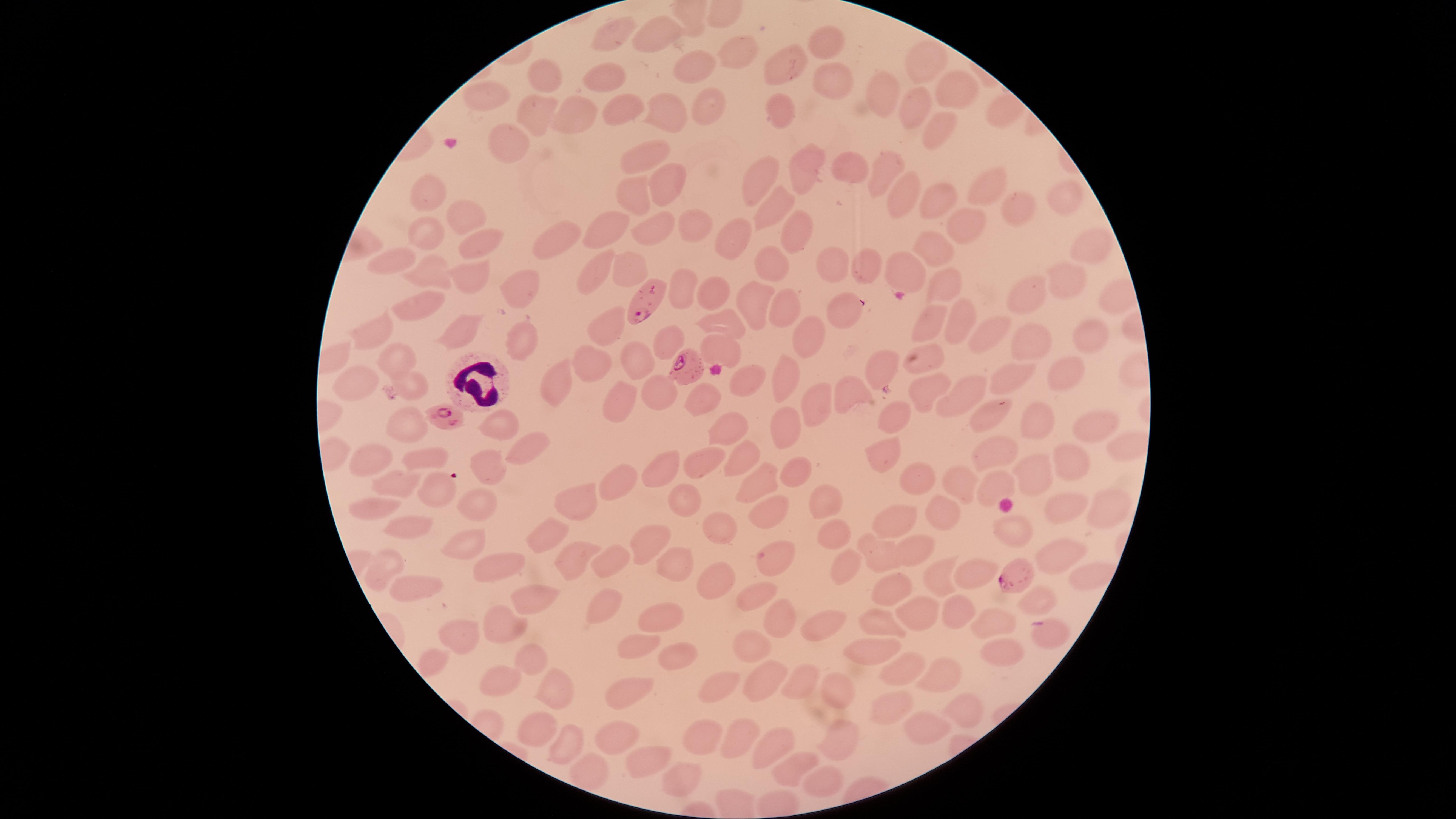

Approximate marker points as [x, y] in pixels.
Summary:
  - Parasitized red blood cells: [648, 298], [684, 366], [442, 417], [1012, 577]
  - White blood cells: [476, 381]
  - Uninfected red blood cells: [611, 31], [658, 34], [827, 41], [738, 51], [785, 66], [697, 69], [925, 69], [609, 76], [541, 77], [828, 79], [954, 88], [873, 96], [494, 100], [918, 106], [706, 108], [622, 111], [579, 112], [782, 112], [664, 113], [541, 114], [932, 127], [512, 145], [640, 156], [806, 165], [852, 167], [877, 168], [760, 174], [666, 185], [980, 188], [902, 189], [430, 192], [633, 193], [1064, 199], [934, 202], [775, 206], [1016, 208], [457, 217], [602, 223], [695, 223], [961, 229], [426, 232], [654, 232], [798, 234], [481, 238], [734, 238], [555, 241], [941, 242], [1084, 246], [393, 258], [838, 265], [629, 267], [777, 267], [863, 269], [597, 270], [432, 271], [900, 271], [1067, 275], [468, 281], [518, 284], [715, 285], [683, 287], [950, 287], [1027, 292], [414, 298], [754, 298], [787, 303], [844, 311], [726, 317], [925, 320], [953, 321], [607, 324], [378, 329], [458, 333], [986, 333], [1088, 338], [806, 339], [521, 341], [666, 341], [1023, 344], [725, 346], [593, 358], [635, 359], [924, 361], [399, 362], [885, 365], [1066, 375], [786, 378], [364, 380], [413, 380], [557, 380], [749, 380], [1003, 380], [925, 386], [852, 393], [659, 395], [962, 395], [822, 396], [700, 398], [614, 399], [894, 413], [996, 417], [1039, 420], [1098, 424], [406, 425], [501, 425], [728, 427], [789, 428], [531, 445], [1120, 447], [994, 450], [882, 455], [743, 457], [421, 459], [370, 460], [1068, 462], [698, 463], [489, 468], [655, 469], [792, 471], [1040, 477], [757, 478], [914, 480], [608, 483], [997, 485], [962, 486], [399, 487], [434, 488], [685, 497], [825, 497], [577, 501], [477, 504], [1062, 507], [365, 509], [765, 512], [1104, 512], [943, 513], [711, 525], [414, 526], [893, 527], [1017, 530], [832, 532], [545, 537], [650, 538], [459, 544], [917, 550], [878, 551], [1061, 556], [772, 557], [566, 559], [492, 561], [383, 563], [603, 565], [673, 565], [841, 566], [974, 566], [708, 580], [939, 580], [890, 587], [420, 588], [754, 589], [953, 603], [1037, 603], [599, 605], [532, 606], [657, 617], [910, 620], [995, 621], [779, 622], [880, 622], [824, 627], [501, 630], [1051, 634], [456, 635], [630, 649], [1003, 652], [673, 653], [752, 653], [871, 654], [532, 655], [431, 660], [900, 670], [941, 674], [797, 679], [763, 681], [500, 684], [723, 689], [839, 692], [552, 693], [625, 694], [893, 700], [965, 706], [533, 722], [922, 724], [736, 729], [702, 738], [779, 739], [616, 741], [562, 743], [840, 744], [644, 761], [787, 767], [682, 778], [824, 782]
  - Presence: malaria parasites identified
  - Preparation: thin smear of blood
  - Species: Plasmodium falciparum
  - Field of view: single
  - Capture: smartphone photograph through the microscope eyepiece
  - Stain: Giemsa
  - Visible region: circular
  - Image size: 1456×819 pixels